Comment on the morphology of the erythrocytes.
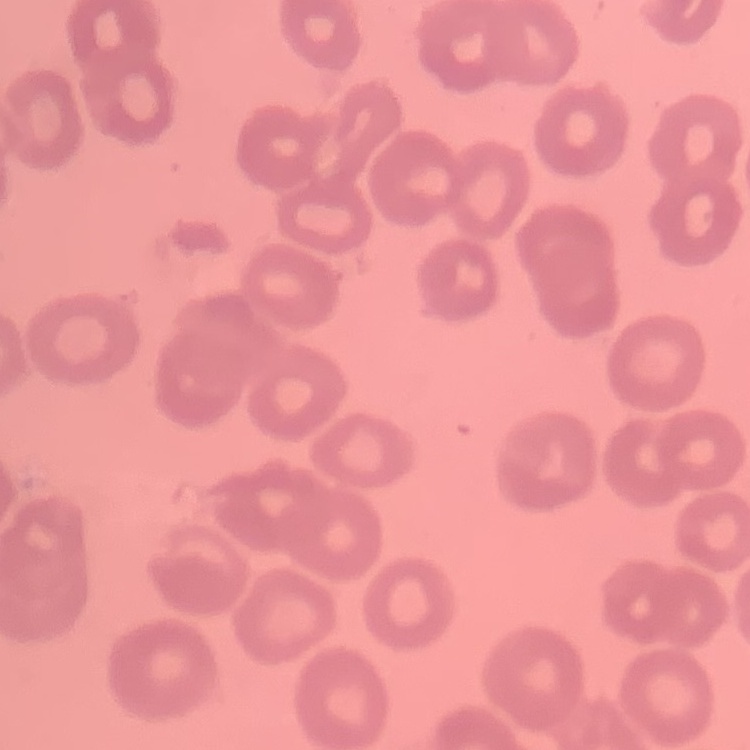
They show no rouleaux formation.

One tile cut from a larger photomicrograph. Thin peripheral smear. Stained with either Field's or Giemsa.